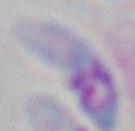 Photomicrograph. 1000x magnification. Toxoplasma gondii is shown.